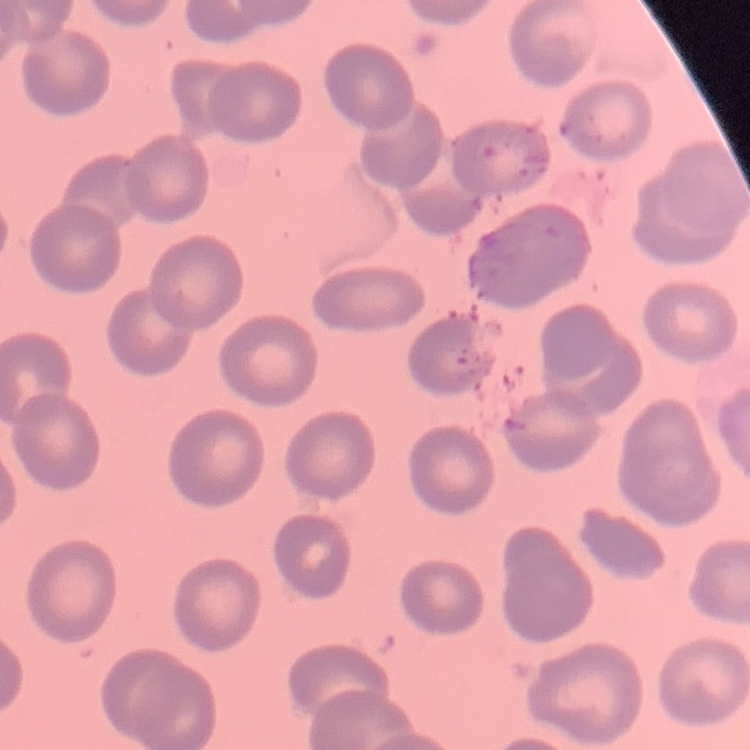

The red blood cells exhibit no rouleaux formation. Thin blood film. Stained with either Field's or Giemsa. Square crop of a larger photomicrograph.